State which parasite is depicted.
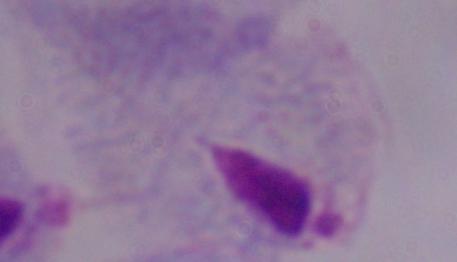
This is a trichomonad.

magnification = 1000x
modality = micrograph